Locate every leukocyte (white blood cell).
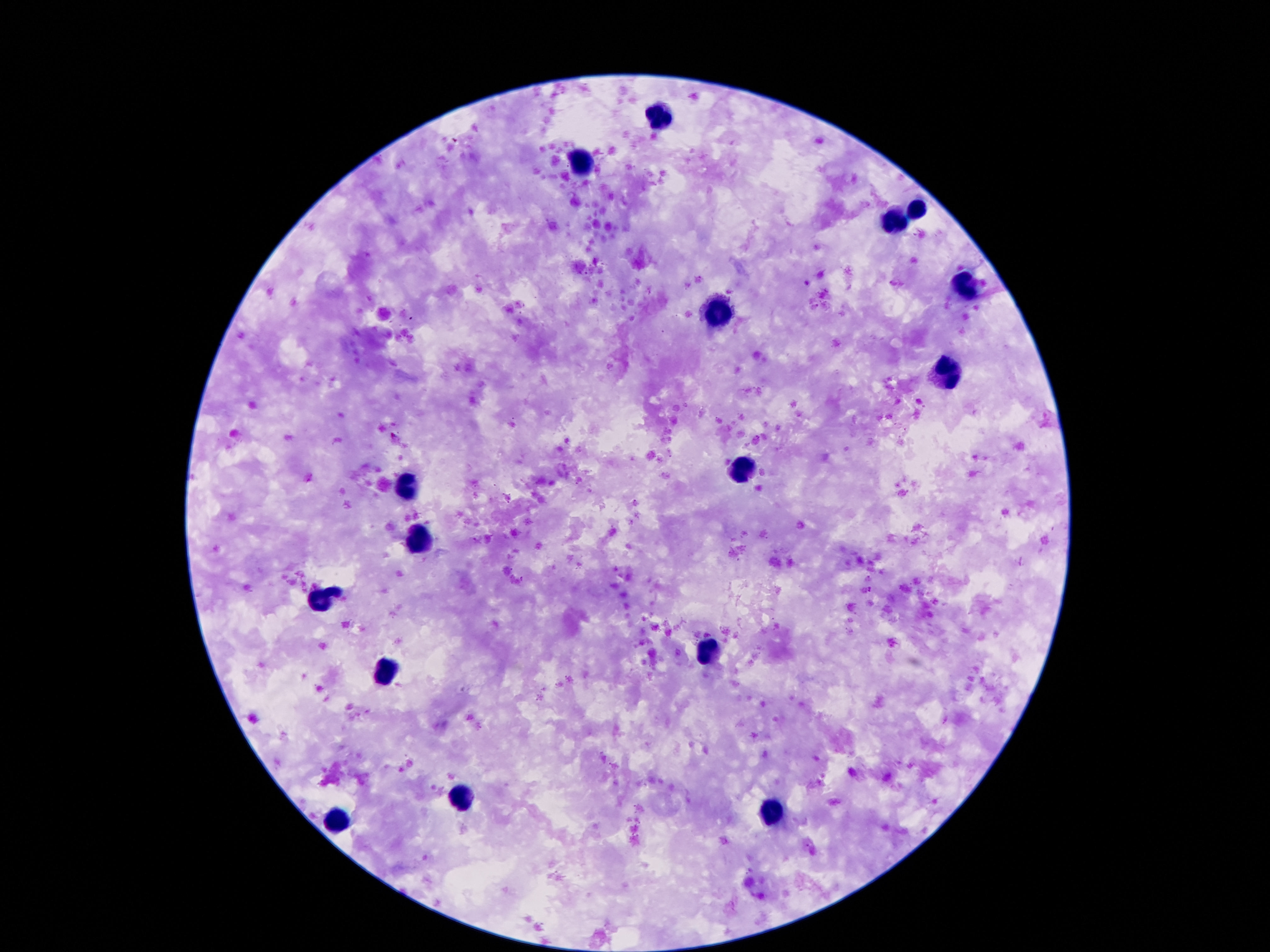

Approximate centers as [x, y] in pixels.
Leukocytes: [658, 116], [580, 162], [920, 208], [891, 221], [968, 284], [716, 311], [945, 376], [737, 473], [403, 488], [420, 540], [324, 600], [706, 652], [380, 675], [460, 799], [771, 813], [338, 822].

field of view = single
magnification = 100x
capture = smartphone camera through the microscope eyepiece
patient malaria status = uninfected
stain = Giemsa
image size = 1270×952 pixels
preparation = thick peripheral-blood smear